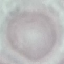

malaria status = uninfected
stain = Giemsa
image type = cell patch, automatically extracted from a larger field of view and resized to 64 × 64 pixels
capture = smartphone through the microscope eyepiece
preparation = thin blood smear